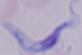

identification = trypanosome
magnification = 1000x
modality = micrograph